State which parasite is depicted.
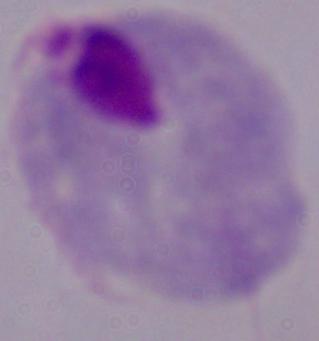

This is a trichomonad.

Summary:
  - Magnification: 1000x
  - Modality: photomicrograph